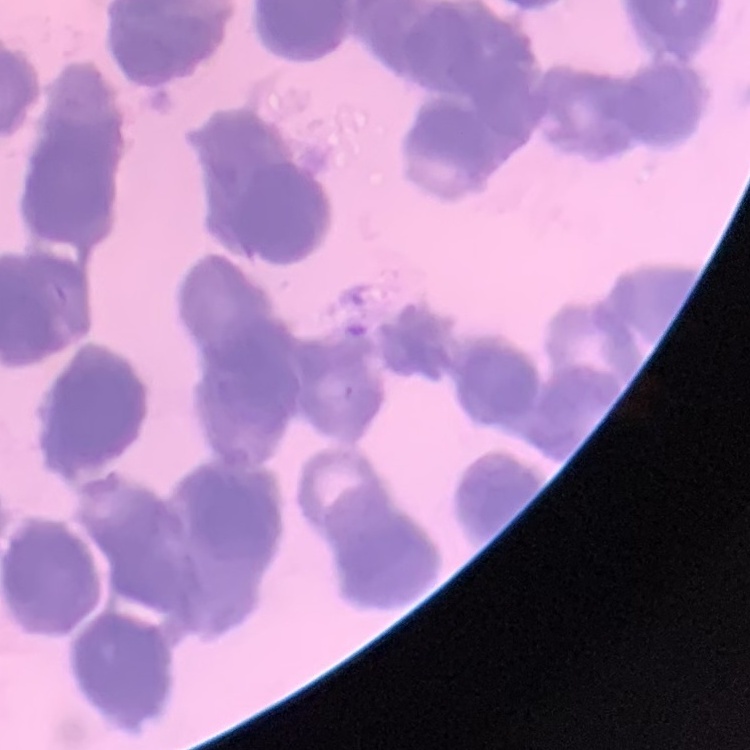

erythrocyte morphology = rouleaux formation
image type = square crop of a larger photomicrograph
stain = Field's or Giemsa
preparation = thin blood smear